Outline each P. falciparum parasite and classify it by life-cycle stage.
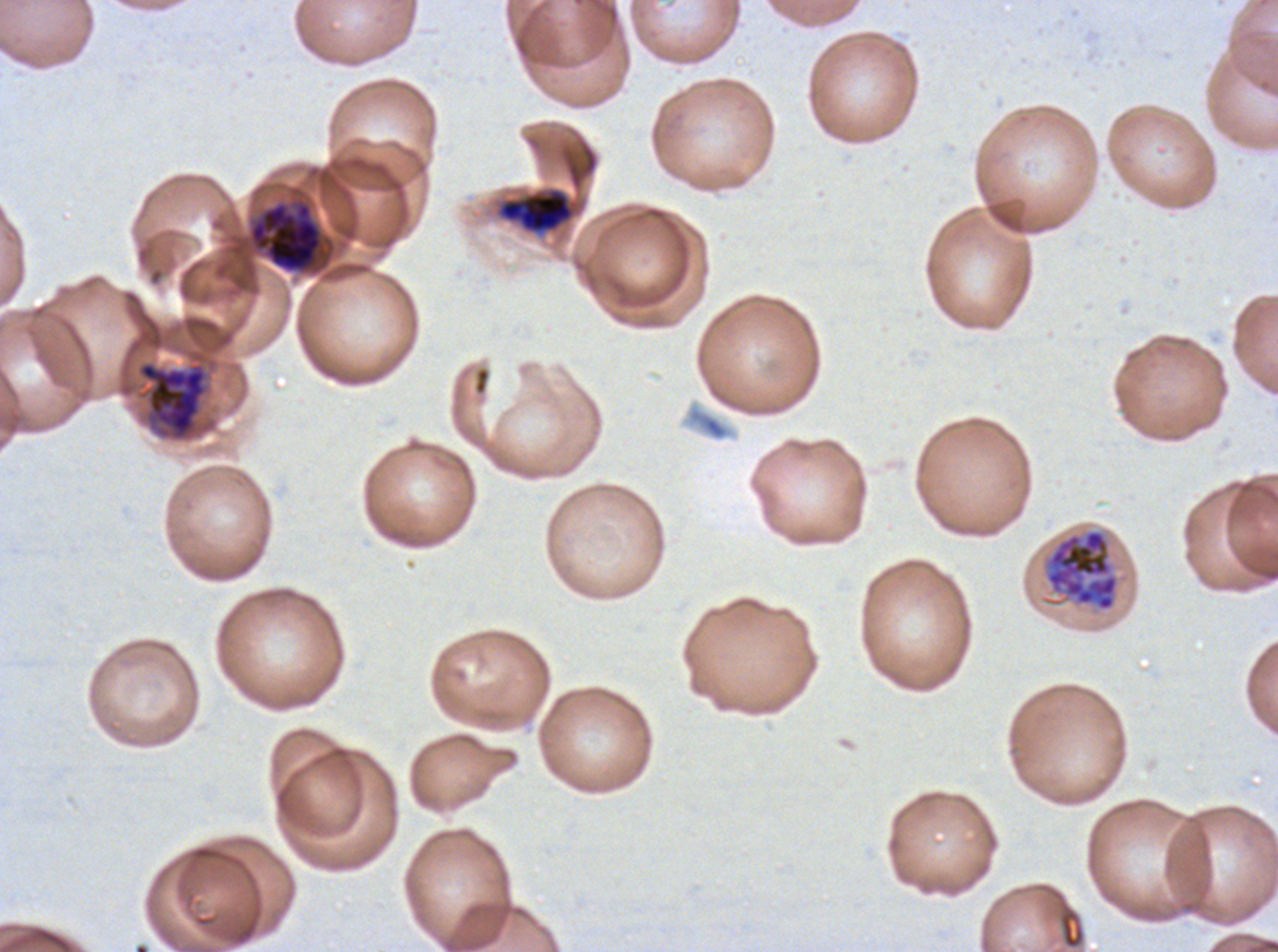
Approximate bounding rectangles given as corner coordinates in pixels from the top-left.
Early schizonts: (x1=498, y1=188, x2=575, y2=234), (x1=1045, y1=529, x2=1119, y2=612).
Late schizonts: (x1=250, y1=203, x2=322, y2=272), (x1=138, y1=361, x2=207, y2=439).
No rings, late-ring/early-trophozoite forms, mid trophozoites, late trophozoites, segmenters, or gametocytes observed.

P. falciparum from a patient in The Gambia, cultured ex vivo for 24 to 48 hours. Thin blood film. Life-cycle stages observed: early schizont, late schizont. One sub-image of a larger composite. Image is 1278×952 pixels. Giemsa-stained preparation.